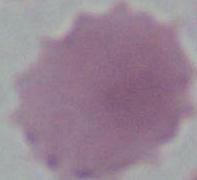
Summary:
  - Identification: erythrocyte
  - Magnification: 1000x
  - Modality: micrograph